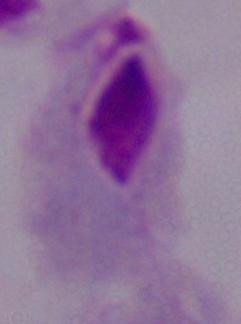

identification = trichomonad
modality = photomicrograph
magnification = 1000x